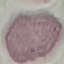

Summary:
  - Result: no malaria parasites seen
  - Stain: Giemsa
  - Preparation: thin blood smear
  - Image type: cell patch, automatically extracted from a larger field of view and resized to 64 × 64 pixels
  - Capture: smartphone camera at the microscope eyepiece